Assess the morphology of the erythrocytes.
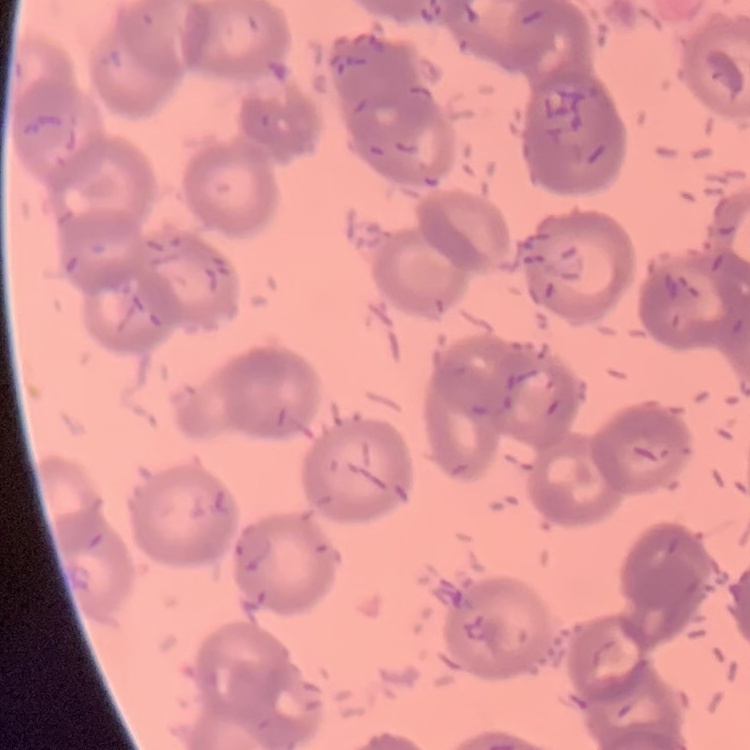
Rouleaux formation.

Stained with either Field's or Giemsa. One tile cut from a larger photomicrograph. Thin peripheral smear.